Identify the cell.
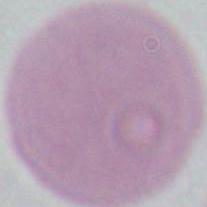

This is an erythrocyte.

Photomicrograph. Captured at 1000x magnification.